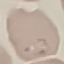
Summary:
  - Malaria status: parasitized
  - Capture: smartphone camera at the microscope eyepiece
  - Preparation: thin blood smear
  - Image type: cell patch, automatically extracted from a larger field of view and resized to 64 × 64 pixels
  - Stain: Giemsa